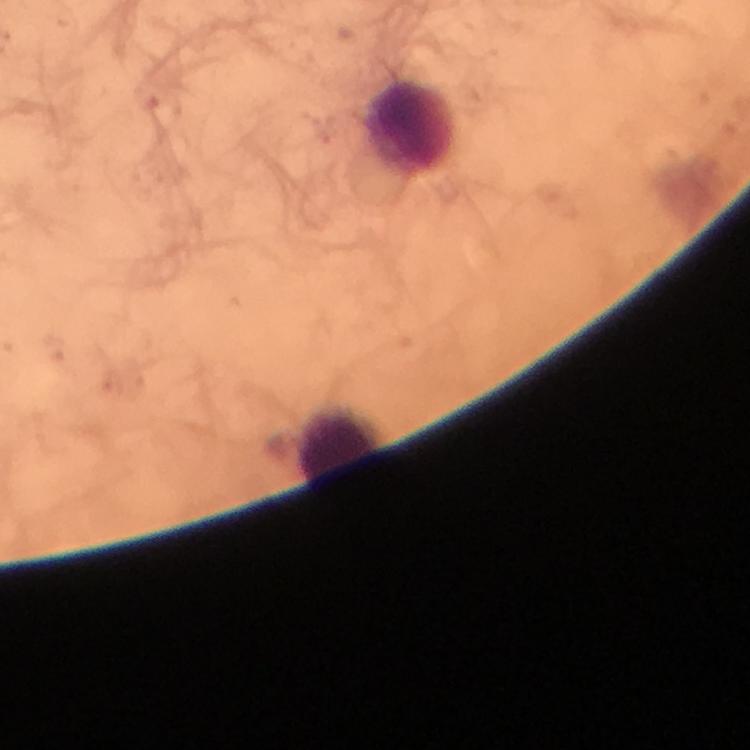
Approximate centers as [x, y] in pixels. Leukocyte locations: [411, 130], [339, 448]. Photographed through the microscope with a smartphone camera. Giemsa stain. Image is 750×750 pixels. Thick blood smear. Cropped region of a single field of view. From a diagnostic examination for malaria. Immersion oil applied. Plasmodium parasites: none seen. 100x magnification.